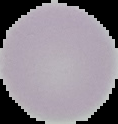

Cell region segmented out of the field of view; the surrounding area is masked to black. Malaria status: uninfected. Image is 118×124 pixels. From a thin blood film.